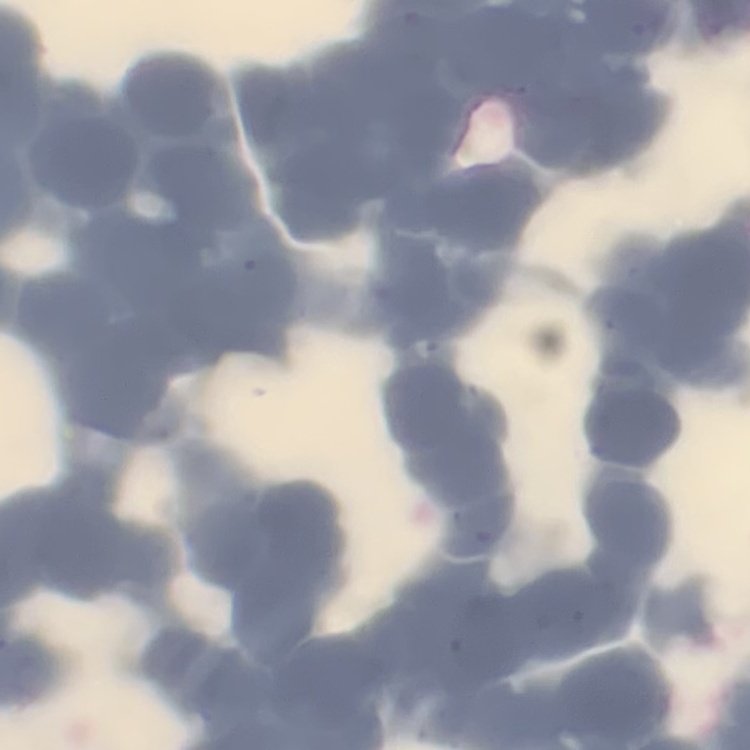 The red blood cells exhibit rouleaux formation. Thin blood smear. Square crop of a larger photomicrograph. Stained with either Field's or Giemsa.